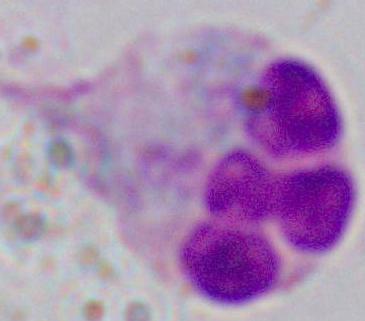

Summary:
  - Modality: micrograph
  - Magnification: 1000x
  - Identification: white blood cell